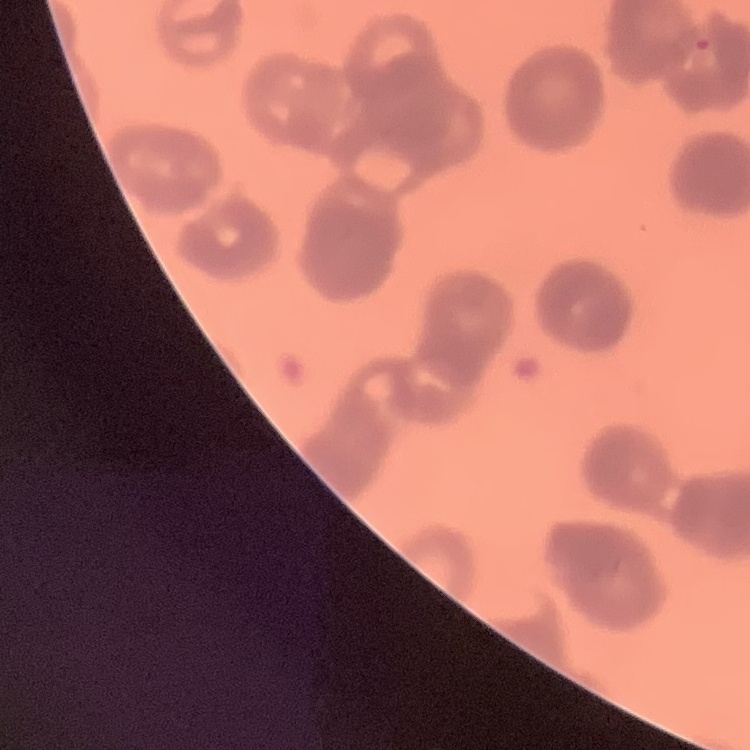

red_blood_cell_morphology: rouleaux formation
preparation: thin blood film
stain: Field's or Giemsa
image_type: square crop of a larger photomicrograph